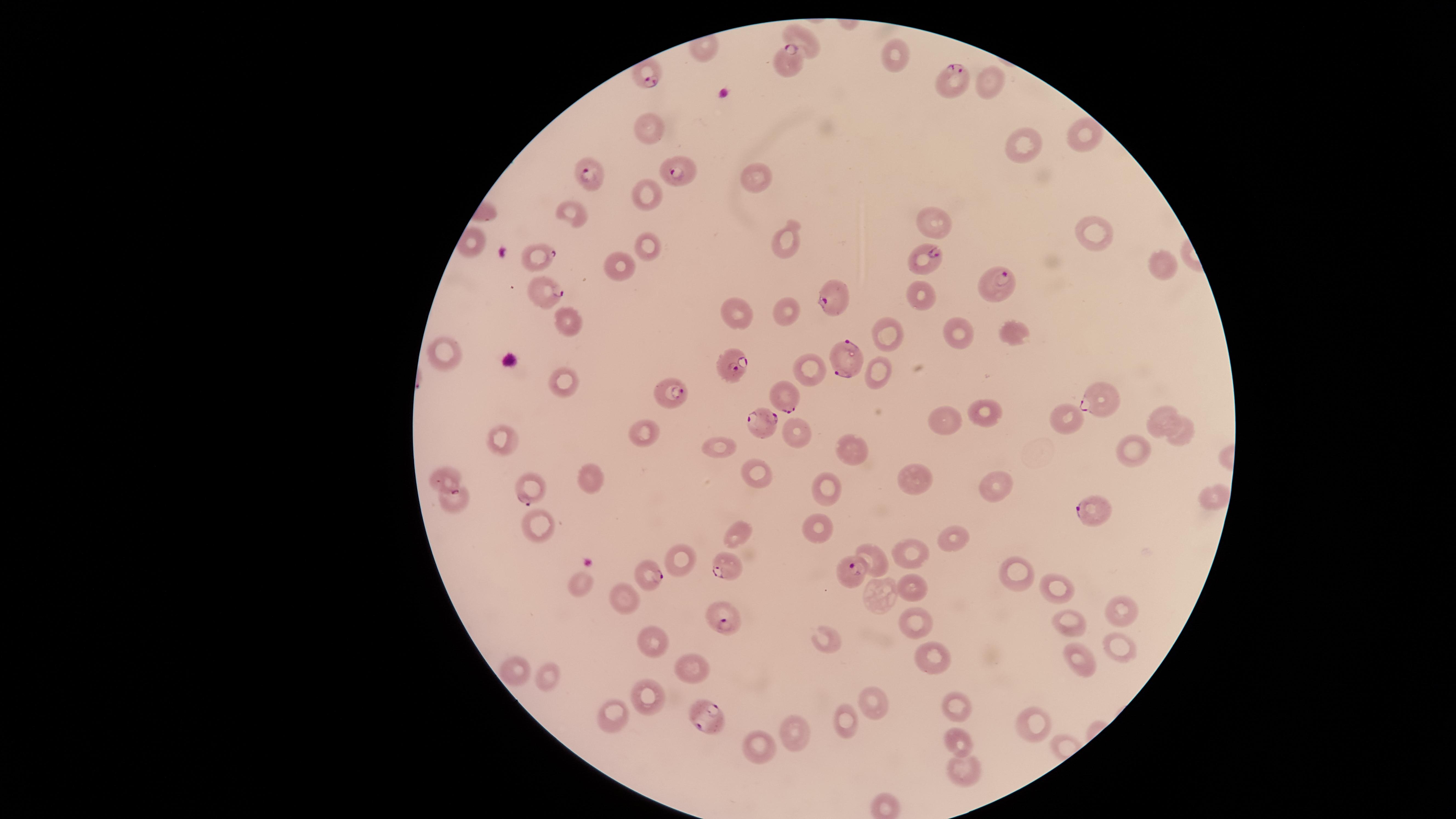
Approximate marker points, in pixels from the top-left corner. Parasitized red blood cells: (x=789, y=64), (x=648, y=70), (x=951, y=80), (x=588, y=171), (x=680, y=171), (x=537, y=252), (x=924, y=260), (x=539, y=291), (x=995, y=291), (x=832, y=299), (x=845, y=359), (x=730, y=367), (x=784, y=391), (x=672, y=397), (x=1097, y=397), (x=765, y=427), (x=441, y=476), (x=530, y=488), (x=1093, y=510), (x=723, y=566), (x=848, y=569), (x=648, y=572), (x=721, y=616), (x=703, y=715). Uninfected red blood cells: (x=803, y=35), (x=992, y=79), (x=650, y=120), (x=1086, y=134), (x=1019, y=139), (x=755, y=178), (x=641, y=193), (x=577, y=214), (x=936, y=217), (x=1095, y=231), (x=785, y=239), (x=648, y=243), (x=619, y=263), (x=1163, y=264), (x=916, y=290), (x=735, y=308), (x=786, y=309), (x=570, y=319), (x=958, y=328), (x=883, y=329), (x=1006, y=330), (x=446, y=353), (x=810, y=363), (x=878, y=363), (x=565, y=382), (x=980, y=410), (x=1060, y=415), (x=1158, y=415), (x=943, y=417), (x=1187, y=427), (x=649, y=431), (x=499, y=434), (x=797, y=435), (x=721, y=447), (x=1132, y=447), (x=849, y=455), (x=753, y=467), (x=918, y=474), (x=589, y=475), (x=991, y=482), (x=833, y=489), (x=1217, y=497), (x=453, y=501), (x=537, y=525), (x=818, y=525), (x=734, y=530), (x=950, y=538), (x=869, y=551), (x=903, y=553), (x=684, y=558), (x=1017, y=572), (x=913, y=580), (x=578, y=585), (x=1055, y=586), (x=881, y=595), (x=625, y=598), (x=1119, y=611), (x=1069, y=619), (x=916, y=621), (x=823, y=635), (x=652, y=638), (x=1117, y=647), (x=928, y=655), (x=1080, y=660), (x=688, y=662), (x=509, y=666), (x=558, y=675), (x=652, y=697), (x=875, y=700), (x=961, y=705), (x=617, y=716), (x=1037, y=721), (x=846, y=726), (x=804, y=734), (x=960, y=742), (x=761, y=747), (x=964, y=775). One field of view of the specimen. Thin blood film. Smartphone photograph through the microscope eyepiece. Species: Plasmodium falciparum. Image is 1456×819 pixels. Presence: malaria parasites detected. Circular visible region. Giemsa stain.